Comment on the morphology of the erythrocytes.
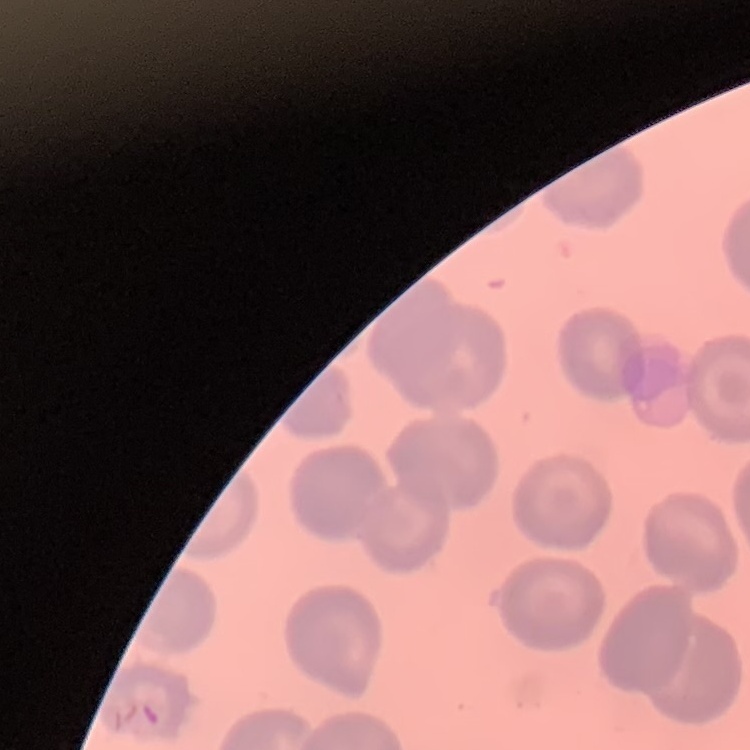

They show no rouleaux formation.

Summary:
  - Preparation: thin peripheral smear
  - Stain: Field's or Giemsa
  - Image type: one tile cut from a larger photomicrograph